Locate every blood parasite and identify its species.
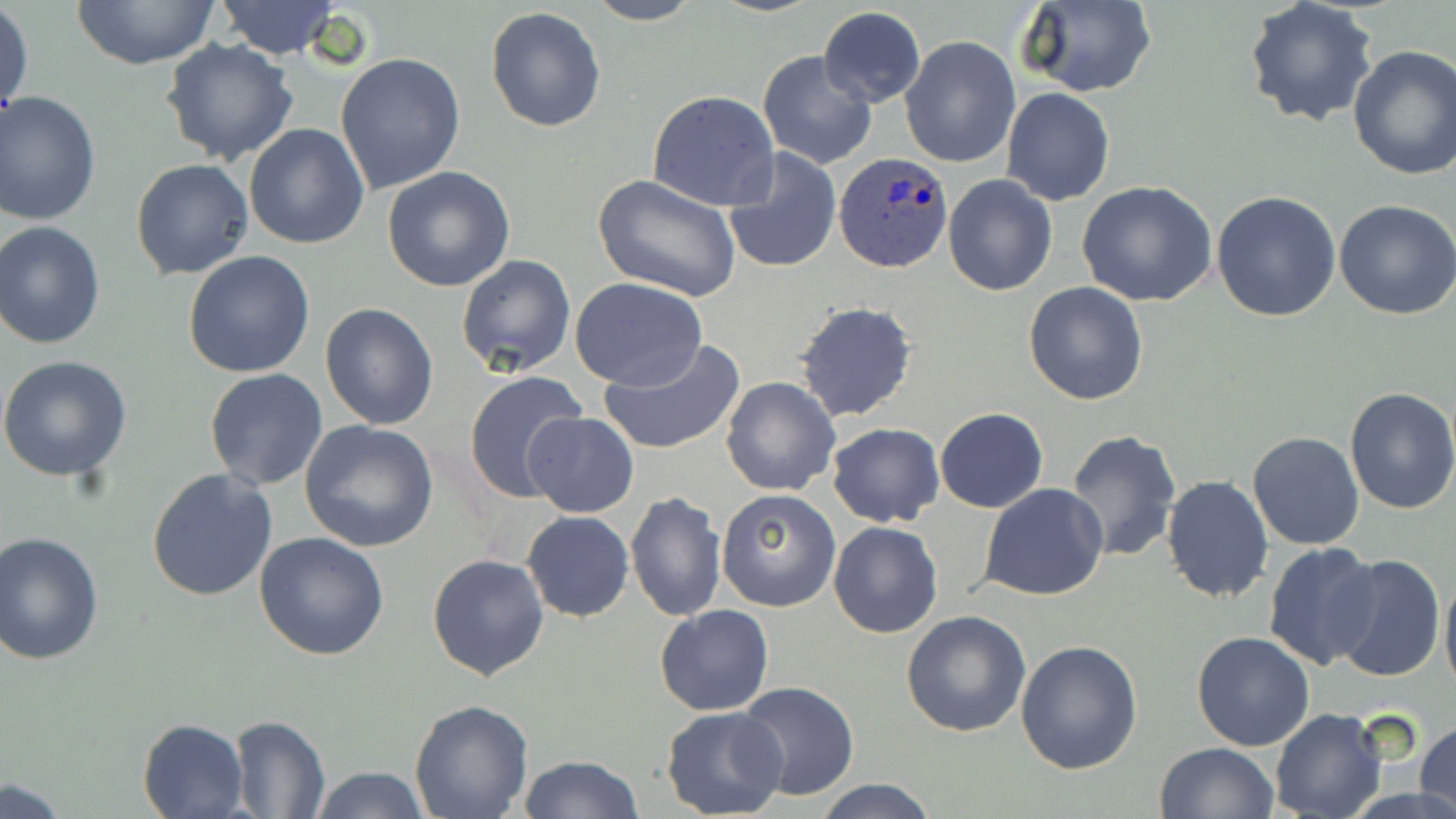
Approximate bounding boxes as (x1, y1, x2, y2) in pixels.
Plasmodium ovale-infected red blood cells: (834, 152, 954, 273).
No Plasmodium falciparum, Plasmodium malariae, Plasmodium vivax, Babesia divergens, or Trypanosoma brucei observed.

slide-level diagnosis = Plasmodium ovale
stain = May-Grünwald-Giemsa
field of view = one of a larger specimen
uninfected red blood cell locations = approximate bounding boxes as (x1, y1, x2, y2) in pixels: (71, 0, 222, 69), (583, 0, 704, 25), (1016, 0, 1157, 98), (213, 1, 343, 59), (1243, 1, 1378, 129), (1, 4, 34, 124), (485, 5, 607, 133), (818, 7, 926, 108), (898, 36, 1019, 169), (160, 38, 301, 169), (1346, 46, 1456, 180), (757, 49, 877, 170), (335, 53, 466, 196), (1002, 89, 1115, 206), (646, 91, 779, 211), (0, 92, 101, 225), (243, 122, 369, 250), (723, 148, 842, 275), (130, 158, 253, 279), (382, 166, 516, 292), (593, 174, 740, 301), (942, 174, 1059, 295), (1076, 179, 1218, 307), (1212, 191, 1343, 323), (1334, 199, 1456, 319), (0, 221, 107, 349), (183, 250, 315, 377), (456, 253, 577, 377), (570, 277, 707, 389), (1023, 281, 1149, 405), (793, 301, 919, 424), (319, 302, 440, 431), (599, 339, 746, 455), (0, 354, 132, 483), (204, 369, 329, 491), (462, 371, 588, 505), (720, 377, 840, 497), (1342, 386, 1456, 515), (933, 409, 1049, 512), (523, 412, 638, 518), (298, 419, 441, 553), (827, 422, 943, 527), (1064, 429, 1181, 561), (1247, 431, 1364, 550), (146, 467, 278, 599), (1160, 474, 1275, 603), (980, 484, 1109, 601), (715, 488, 839, 611), (626, 492, 725, 622), (522, 511, 634, 623), (828, 520, 943, 638), (0, 531, 104, 666), (255, 532, 389, 661), (1263, 541, 1383, 669), (427, 553, 548, 681), (1331, 554, 1445, 685), (1439, 564, 1456, 701), (654, 604, 774, 716), (902, 609, 1031, 737), (1191, 632, 1315, 751), (1016, 639, 1144, 775), (734, 681, 861, 801), (408, 698, 534, 818), (660, 706, 788, 818), (1269, 709, 1389, 819), (227, 715, 330, 818), (137, 717, 251, 819), (1416, 719, 1456, 818), (1155, 742, 1278, 819), (517, 755, 643, 819), (309, 765, 431, 819), (814, 778, 941, 818), (0, 779, 70, 818)
image size = 1456×819 pixels
preparation = thin blood smear
magnification = 1000x
modality = optical microscopy